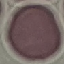

Summary:
  - Malaria status: uninfected
  - Image type: cell patch, automatically extracted from a larger field of view and resized to 64 × 64 pixels
  - Preparation: thin blood smear
  - Stain: Giemsa
  - Capture: smartphone through the microscope eyepiece